Describe the morphology of the red blood cells.
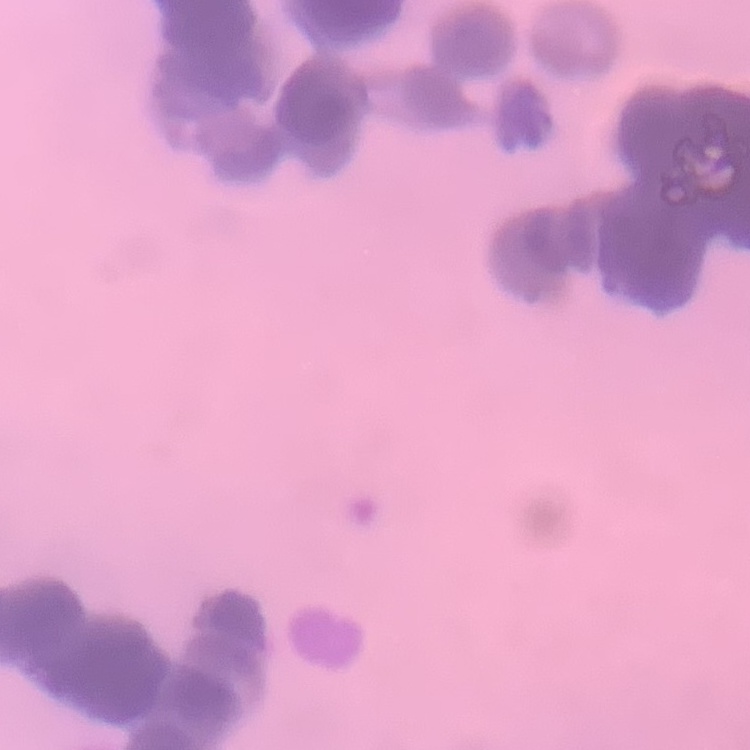
Rouleaux formation.

Summary:
  - Preparation: thin blood film
  - Stain: Field's or Giemsa
  - Image type: one tile cut from a larger photomicrograph